Report the malaria status of this cell.
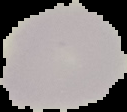
It is uninfected.

From a thin blood film. Segmented cell region on a black background. Image is 127×112 pixels.